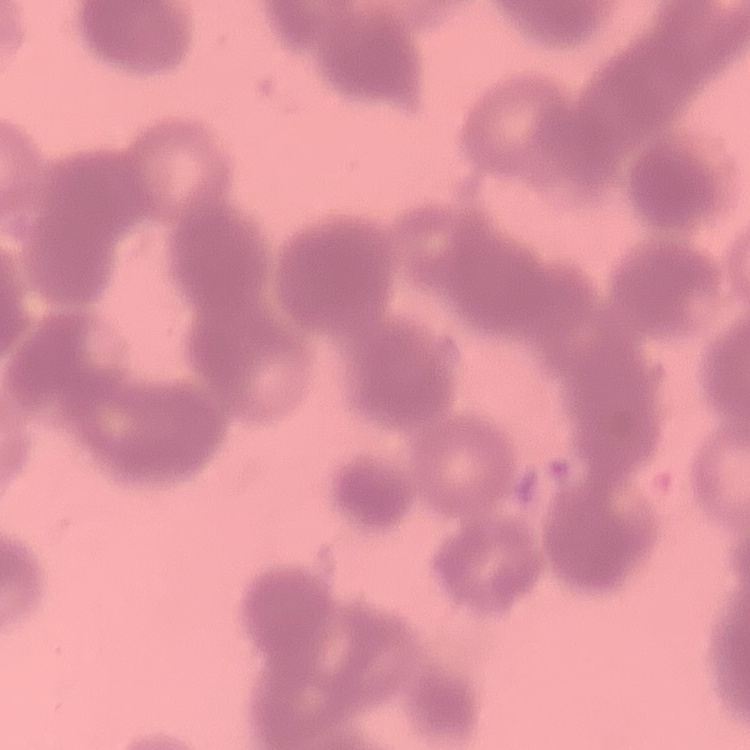 The red blood cells show rouleaux formation. Square crop of a larger photomicrograph. Thin blood smear. Field's or Giemsa stain.